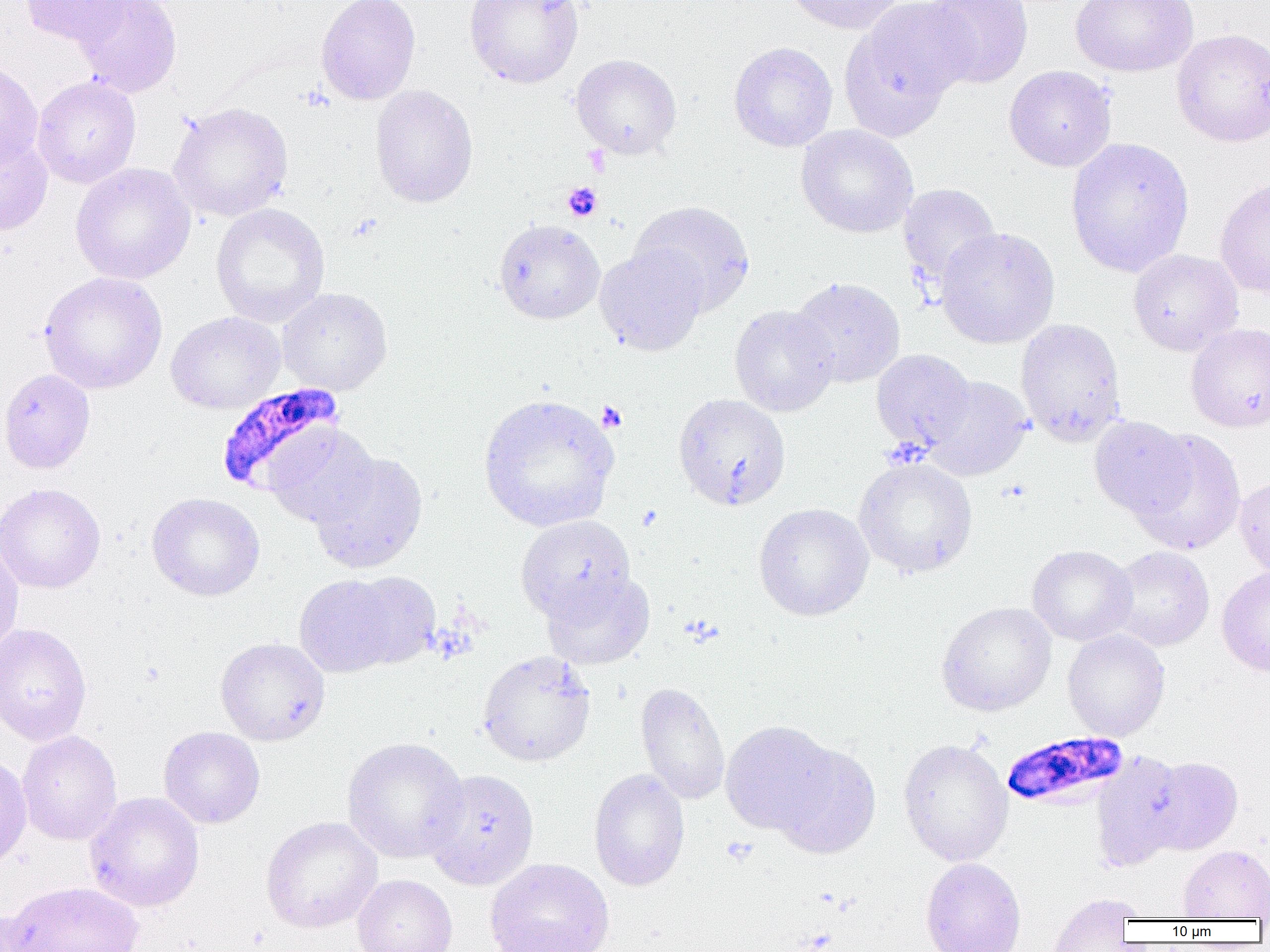

Approximate bounding boxes as [x1, y1, x2, y2] in pixels. Uninfected red blood cell locations: [20, 0, 133, 48], [71, 0, 182, 97], [316, 0, 421, 105], [464, 0, 584, 89], [782, 0, 906, 34], [921, 0, 1034, 89], [1069, 0, 1199, 78], [842, 2, 970, 136], [1171, 28, 1270, 147], [728, 42, 838, 152], [571, 54, 682, 159], [0, 59, 43, 168], [1004, 66, 1117, 171], [32, 76, 141, 188], [369, 84, 479, 208], [168, 102, 293, 221], [795, 125, 918, 238], [0, 129, 53, 235], [1065, 137, 1195, 278], [70, 162, 196, 285], [1214, 177, 1270, 299], [897, 183, 1001, 289], [629, 200, 755, 316], [211, 203, 330, 328], [493, 219, 605, 324], [935, 226, 1060, 348], [595, 245, 708, 356], [1128, 249, 1243, 355], [38, 271, 168, 395], [789, 277, 906, 388], [277, 287, 392, 395], [729, 304, 838, 417], [165, 311, 285, 414], [1015, 318, 1126, 446], [1185, 322, 1270, 433], [871, 349, 976, 452], [0, 368, 95, 474], [922, 376, 1033, 481], [478, 393, 619, 532], [673, 393, 791, 511], [1089, 416, 1196, 522], [264, 424, 379, 528], [1130, 428, 1246, 555], [309, 450, 428, 574], [853, 457, 978, 578], [1234, 475, 1270, 582], [0, 483, 106, 594], [146, 492, 265, 601], [753, 503, 874, 621], [515, 515, 635, 622], [0, 538, 24, 656], [1027, 544, 1137, 646], [1106, 546, 1214, 651], [1216, 566, 1270, 676], [344, 571, 441, 670], [540, 571, 655, 670], [294, 574, 403, 678], [936, 602, 1057, 716], [0, 623, 92, 746], [1062, 629, 1170, 741], [215, 637, 330, 746], [477, 649, 596, 767], [635, 681, 730, 805], [720, 720, 839, 836], [158, 726, 265, 829], [17, 730, 123, 845], [341, 737, 469, 864], [898, 738, 1013, 866], [770, 743, 882, 858], [1090, 751, 1188, 872], [0, 753, 32, 871], [1144, 756, 1242, 855], [422, 768, 539, 889], [588, 768, 690, 891], [84, 792, 205, 912], [260, 816, 383, 934], [1178, 845, 1270, 920], [484, 858, 614, 952], [920, 858, 1027, 952], [351, 874, 457, 952], [4, 881, 142, 952], [1046, 893, 1140, 952], [0, 910, 48, 952]. Platelet locations: [582, 145, 610, 176], [562, 182, 603, 222], [596, 401, 627, 432], [721, 836, 758, 865]. Plasmodium falciparum-infected red blood cell locations: [216, 381, 346, 493], [1002, 732, 1128, 810]. Slide-level diagnosis: Plasmodium falciparum. Image is 1270×952 pixels. Light microscopy. Thin blood smear. Single field of view. 1000x magnification.